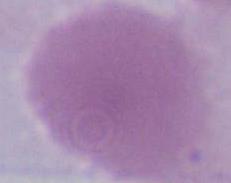

{
  "magnification": "1000x",
  "identification": "erythrocyte",
  "modality": "photomicrograph"
}